Comment on the morphology of the erythrocytes.
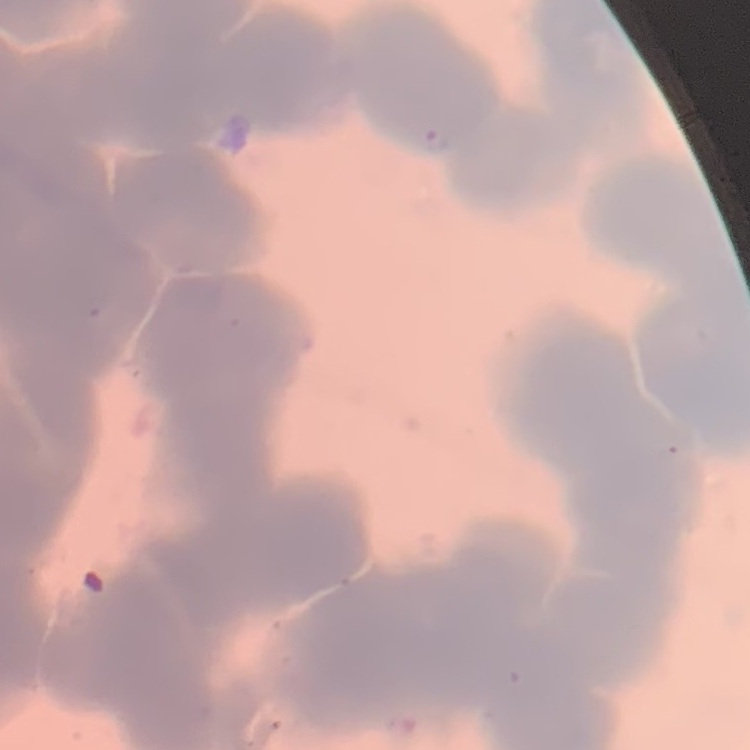
Rouleaux formation.

Summary:
  - Image type: one tile cut from a larger photomicrograph
  - Preparation: thin peripheral smear
  - Stain: Field's or Giemsa